Name the blood parasite species.
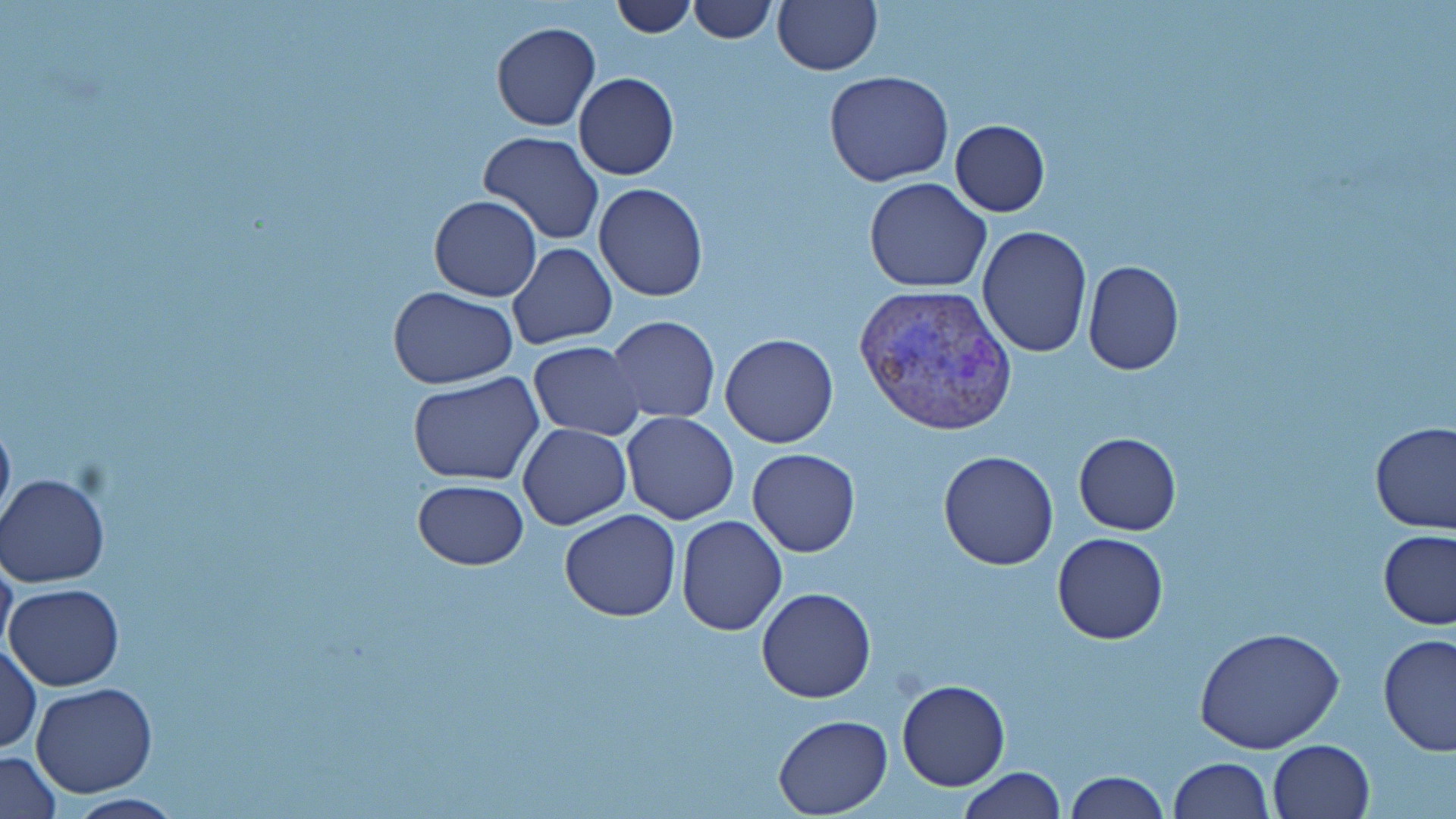

Plasmodium vivax.

Summary:
  - Coordinate format: approximate bounding boxes as (x1,y1)-(x2,y2) corner pairs in pixels
  - Plasmodium vivax-infected red blood cell locations: (855,281)-(1017,438)
  - Uninfected red blood cell locations: (610,0)-(697,37), (688,0)-(776,43), (771,0)-(883,76), (491,23)-(600,131), (824,71)-(953,187), (572,72)-(679,180), (949,120)-(1051,216), (476,131)-(604,244), (864,177)-(992,293), (594,182)-(708,301), (429,194)-(543,301), (977,226)-(1092,360), (506,244)-(617,349), (1082,259)-(1184,375), (389,286)-(517,388), (606,316)-(721,423), (718,332)-(840,448), (527,340)-(645,440), (407,371)-(544,487), (0,407)-(15,533), (621,412)-(740,525), (518,422)-(631,529), (1371,422)-(1456,533), (1075,433)-(1180,533), (747,448)-(860,558), (938,450)-(1059,570), (2,471)-(114,588), (411,480)-(531,569), (558,510)-(681,622), (676,515)-(786,636), (1377,528)-(1455,629), (1051,532)-(1169,644), (0,547)-(18,667), (6,582)-(124,690), (756,586)-(876,704), (1196,628)-(1344,757), (1377,633)-(1455,756), (1,640)-(41,756), (896,678)-(1010,791), (31,683)-(157,798), (772,715)-(891,817), (1267,738)-(1375,819), (1,750)-(61,819), (1168,757)-(1273,818), (958,767)-(1066,818), (1062,770)-(1168,819), (57,792)-(190,819)
  - Preparation: thin blood smear
  - Magnification: 1000x
  - Image size: 1456×819 pixels
  - Field of view: one of a larger specimen
  - Stain: May-Grünwald-Giemsa
  - Modality: light microscopy